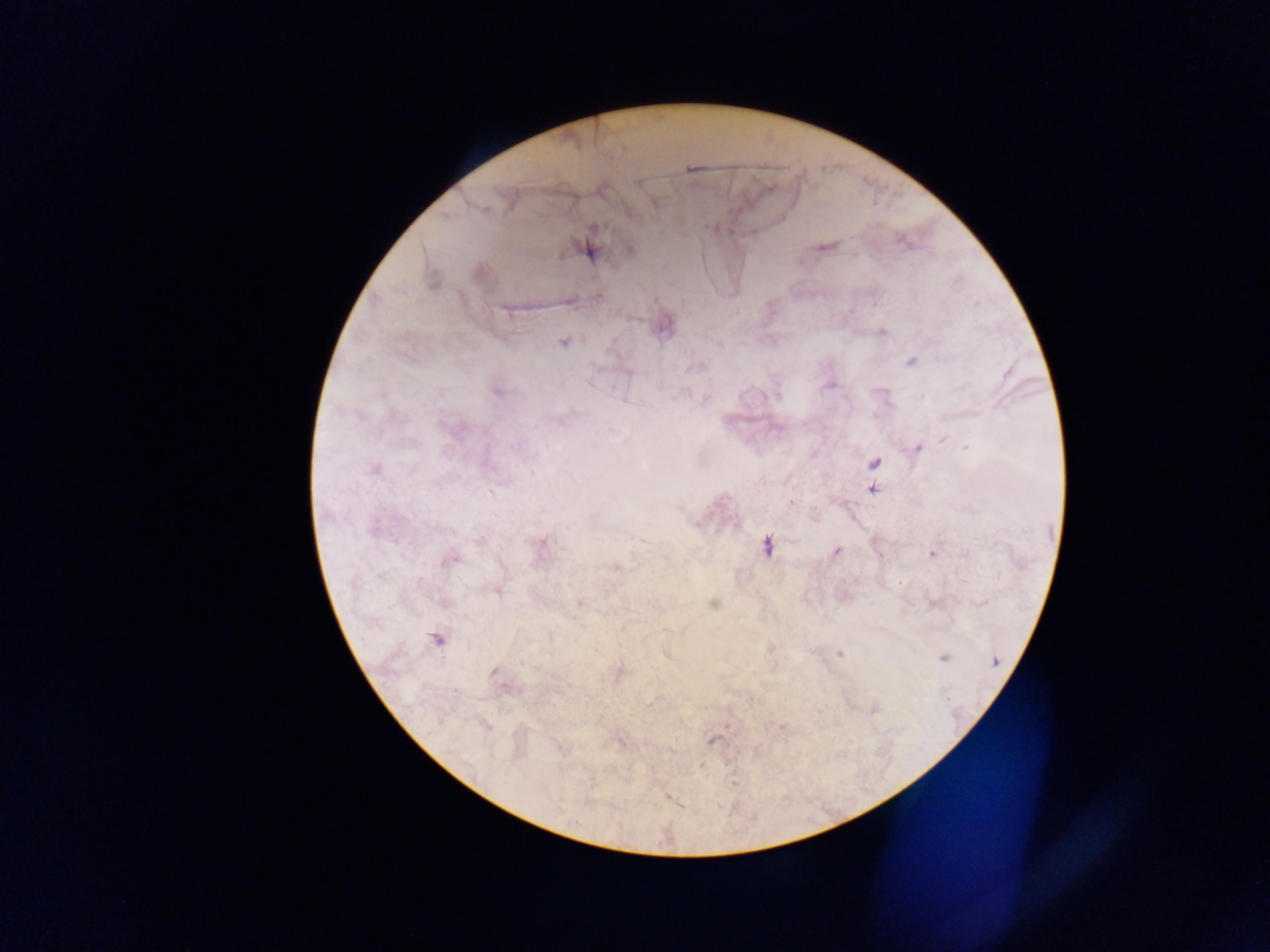
Approximate centers as {x, y} in pixels. Plasmodium parasite locations: {690, 168}, {637, 183}, {653, 203}, {825, 247}, {587, 250}, {629, 250}, {598, 296}, {661, 325}, {881, 331}, {562, 342}, {911, 361}, {829, 384}, {498, 390}, {917, 448}, {873, 463}, {374, 469}, {872, 488}, {790, 503}, {814, 518}, {539, 545}, {766, 545}, {836, 551}, {932, 552}, {448, 559}, {614, 566}, {496, 589}, {579, 602}, {934, 603}, {713, 604}, {437, 639}, {667, 653}, {840, 653}, {942, 657}, {618, 672}, {496, 674}, {484, 724}, {711, 739}, {621, 741}, {559, 746}, {668, 796}. One field of view. Sample from Ghana. Mobile-phone photograph taken through the microscope. Image is 1270×952 pixels. Thick blood film.